Outline each Plasmodium falciparum-infected red blood cell.
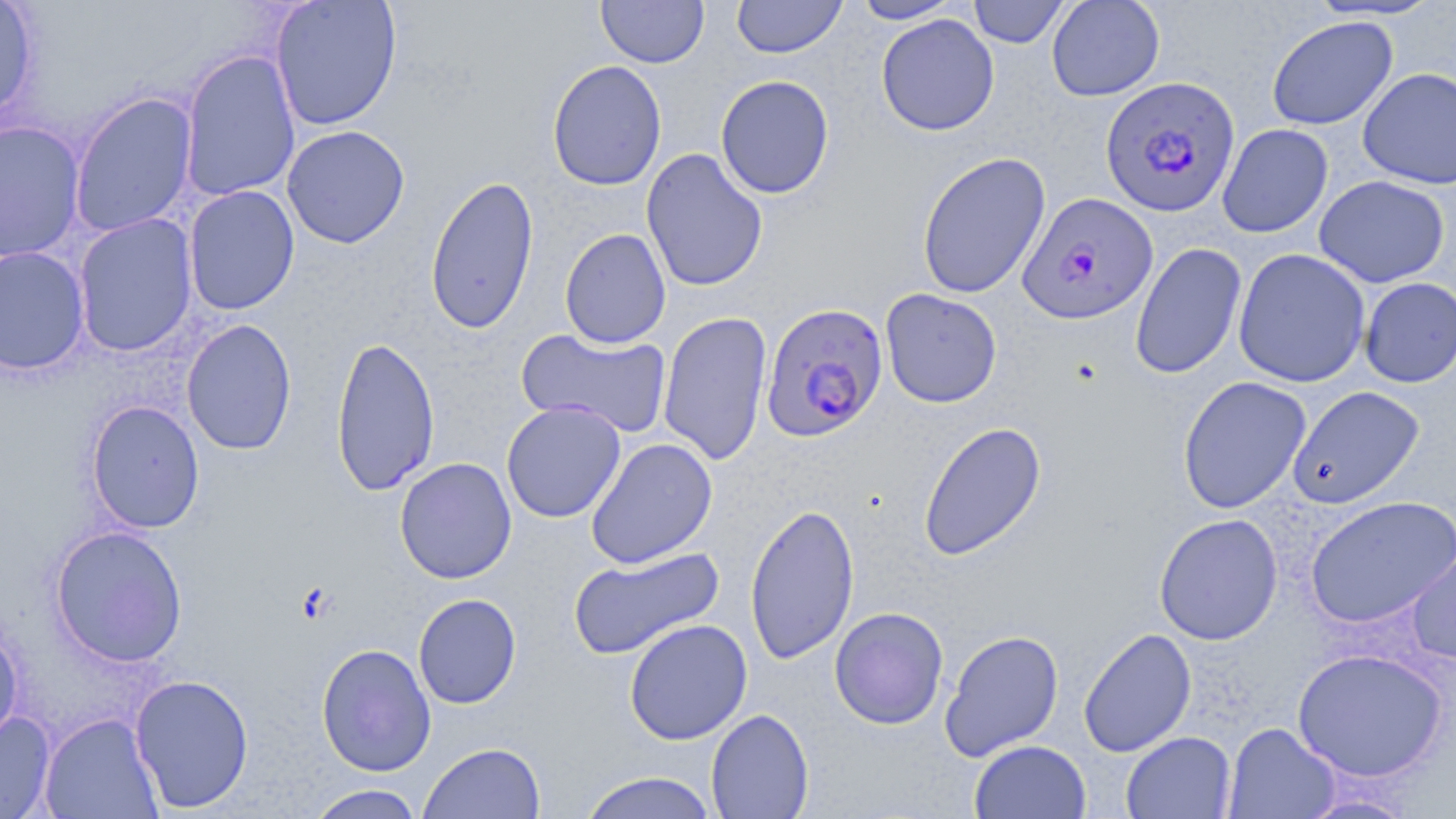
Approximate bounding boxes as (x1,y1)-(x2,y2) corner pairs in pixels.
Plasmodium falciparum-infected red blood cells: (1100,76)-(1240,217), (1016,192)-(1158,325), (759,301)-(889,442).

Summary:
  - Uninfected red blood cell locations: (0,0)-(39,122), (270,0)-(402,130), (596,0)-(709,67), (732,0)-(846,58), (850,0)-(963,24), (967,0)-(1071,48), (1046,0)-(1165,101), (1304,0)-(1445,21), (876,14)-(999,136), (1266,16)-(1398,130), (178,49)-(301,202), (547,60)-(668,191), (1358,67)-(1456,189), (715,74)-(835,199), (68,91)-(199,238), (0,120)-(85,262), (1217,123)-(1333,237), (282,125)-(410,249), (641,147)-(768,292), (917,151)-(1051,299), (425,174)-(540,335), (1314,175)-(1450,288), (184,186)-(300,315), (73,213)-(198,356), (559,228)-(671,349), (1130,242)-(1247,380), (0,246)-(91,376), (1232,247)-(1370,388), (1358,277)-(1456,388), (879,288)-(1002,408), (658,310)-(772,466), (181,319)-(297,455), (516,327)-(671,439), (330,335)-(440,496), (1177,376)-(1312,514), (1287,385)-(1425,509), (86,400)-(205,533), (501,401)-(626,524), (918,421)-(1047,561), (585,437)-(718,569), (394,457)-(517,584), (1304,495)-(1456,628), (744,502)-(860,665), (1154,513)-(1283,645), (50,525)-(188,667), (1406,540)-(1456,666), (567,546)-(724,660), (413,593)-(521,709), (829,606)-(948,729), (624,619)-(752,745), (0,622)-(23,748), (1078,627)-(1197,757), (940,628)-(1064,761), (316,643)-(436,777), (1291,647)-(1449,782), (130,673)-(254,812), (706,708)-(814,819), (0,711)-(56,818), (40,712)-(163,818), (1223,722)-(1341,818), (1121,731)-(1236,818), (969,739)-(1091,819), (418,742)-(545,819), (579,771)-(719,819), (306,784)-(426,818), (1296,791)-(1421,818)
  - Slide-level diagnosis: Plasmodium falciparum
  - Preparation: thin blood film
  - Magnification: 1000x
  - Stain: May-Grünwald-Giemsa
  - Modality: light microscopy
  - Image size: 1456×819 pixels
  - Field of view: one of a larger specimen